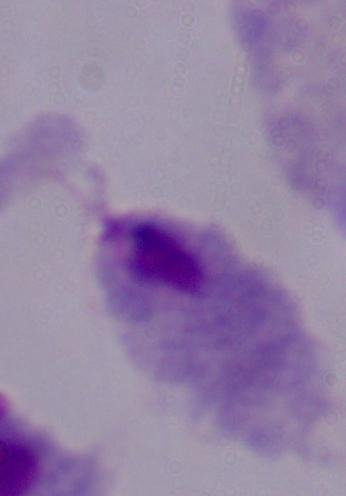

{
  "modality": "photomicrograph",
  "identification": "trichomonad",
  "magnification": "1000x"
}